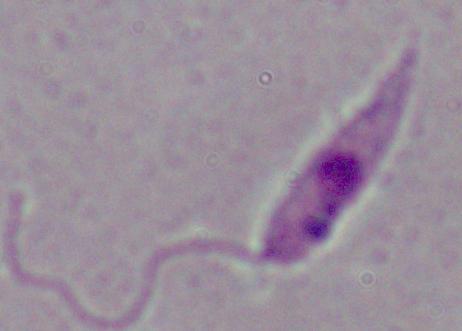

Summary:
  - Magnification: 1000x
  - Identification: Leishmania
  - Modality: photomicrograph